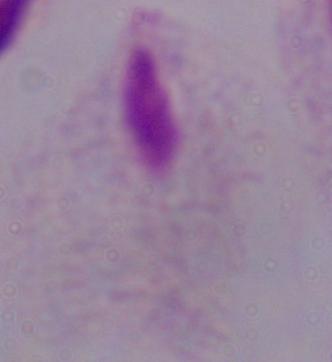
Photomicrograph. A trichomonad is seen. Captured at 1000x magnification.